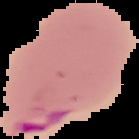

preparation = thin blood film
malaria status = parasitized
image size = 139×139 pixels
image type = segmented cell region on a black background